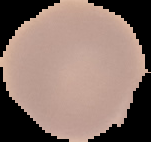

preparation = thin blood film
image size = 151×142 pixels
malaria status = uninfected
image type = cell region segmented out of the field of view; surrounding area masked to black